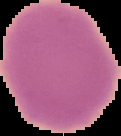

Summary:
  - Malaria status: uninfected
  - Image type: cell region segmented out of the field of view; surrounding area masked to black
  - Preparation: thin blood film
  - Image size: 121×136 pixels